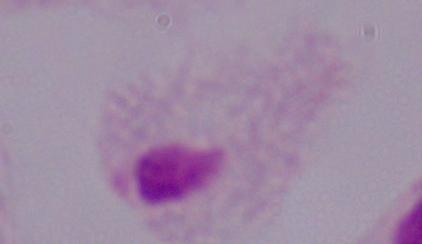
1000x magnification. Micrograph. A trichomonad is shown.